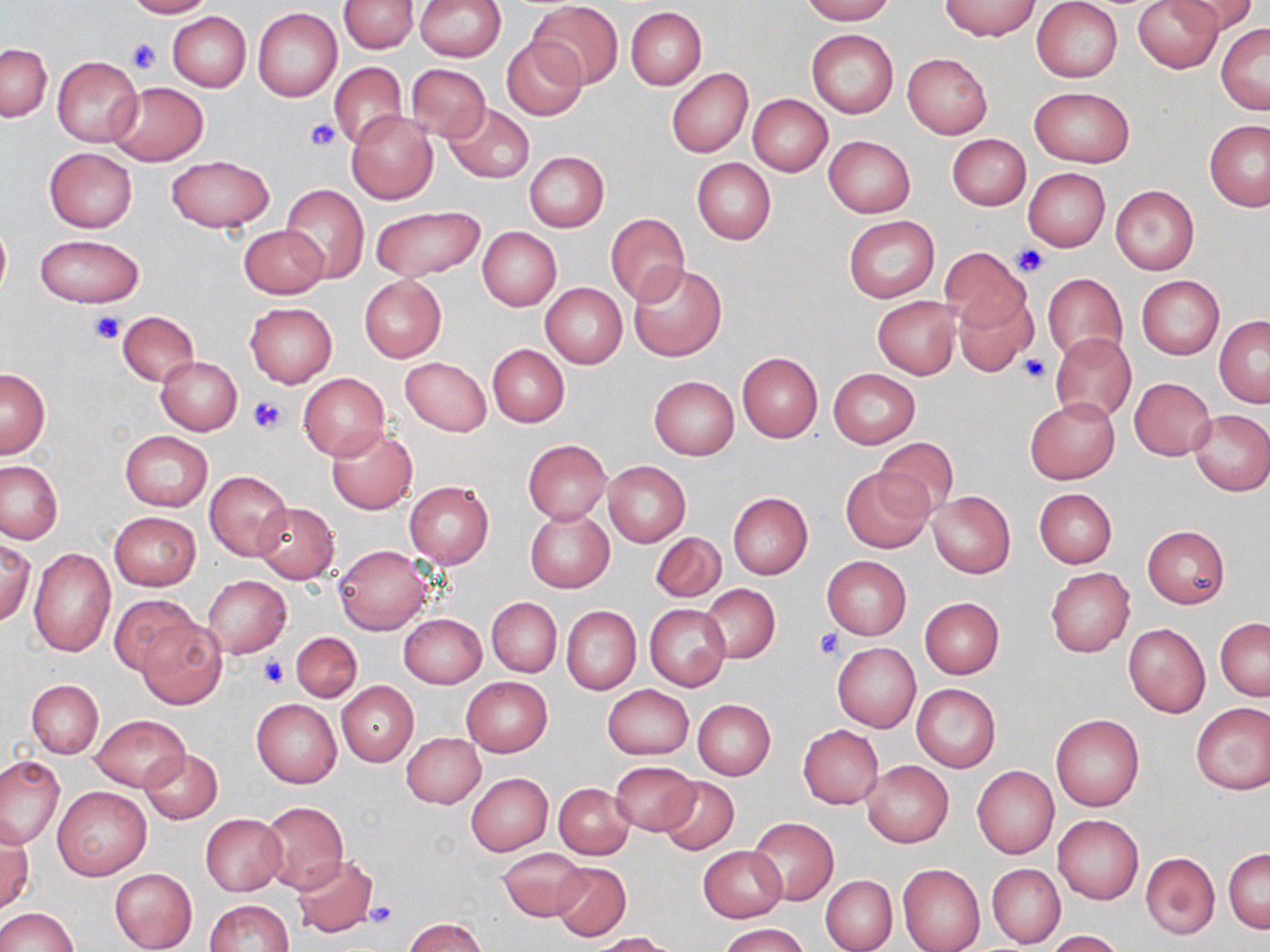
Summary:
  - Coordinate format: approximate bounding boxes as (x1,y1)-(x2,y2) corner pairs in pixels
  - Platelet locations: (124,37)-(163,75), (304,118)-(340,152), (1011,246)-(1048,277), (90,312)-(126,345), (1018,353)-(1051,383), (248,395)-(286,434), (815,629)-(843,659), (258,654)-(288,688), (363,900)-(398,929)
  - Uninfected red blood cell locations: (120,0)-(214,18), (339,0)-(417,54), (415,0)-(506,61), (799,0)-(896,23), (938,0)-(1041,40), (1032,0)-(1122,82), (1132,0)-(1222,73), (1170,0)-(1258,36), (529,1)-(623,88), (626,6)-(705,89), (253,7)-(342,101), (169,13)-(251,91), (1216,23)-(1270,113), (806,29)-(899,119), (501,37)-(587,120), (1,43)-(51,122), (902,52)-(993,139), (52,55)-(143,147), (328,62)-(407,149), (405,63)-(491,142), (666,68)-(753,158), (107,82)-(208,166), (1030,86)-(1134,167), (747,94)-(833,177), (444,102)-(534,185), (347,112)-(437,203), (1204,120)-(1270,210), (947,134)-(1031,211), (823,135)-(916,217), (45,147)-(138,233), (524,152)-(609,232), (165,155)-(275,232), (692,158)-(776,244), (1022,168)-(1110,252), (280,184)-(368,285), (1110,185)-(1199,275), (371,206)-(485,283), (606,213)-(690,306), (843,214)-(939,303), (0,218)-(10,301), (861,219)-(947,377), (239,224)-(329,298), (477,227)-(561,311), (36,234)-(144,308), (939,249)-(1029,329), (627,263)-(726,362), (1043,274)-(1127,361), (359,275)-(446,361), (1136,276)-(1223,358), (540,283)-(627,368), (953,293)-(1036,377), (873,296)-(958,379), (245,303)-(336,387), (115,310)-(199,386), (1214,315)-(1270,407), (1051,335)-(1136,422), (487,344)-(569,426), (737,352)-(822,443), (156,356)-(242,435), (401,356)-(491,437), (0,368)-(49,458), (828,369)-(920,448), (298,372)-(390,461), (649,376)-(740,459), (1130,377)-(1216,460), (1025,398)-(1120,484), (1188,408)-(1270,494), (327,427)-(418,515), (119,430)-(213,511), (874,437)-(960,518), (523,440)-(612,523), (0,460)-(64,544), (603,461)-(690,546), (841,467)-(934,553), (203,470)-(292,560), (403,481)-(493,570), (1034,488)-(1116,568), (928,492)-(1015,578), (728,493)-(812,579), (253,502)-(339,582), (526,508)-(613,593), (110,511)-(200,590), (1142,526)-(1229,608), (650,532)-(725,602), (0,538)-(34,624), (333,545)-(434,634), (28,549)-(115,658), (821,555)-(912,639), (1045,567)-(1135,657), (203,576)-(292,659), (701,584)-(780,663), (109,595)-(201,676), (919,597)-(1004,678), (486,598)-(561,676), (644,604)-(730,691), (561,606)-(641,695), (399,614)-(486,688), (1216,619)-(1270,700), (138,620)-(226,709), (1123,623)-(1210,717), (290,631)-(361,701), (832,642)-(920,732), (462,676)-(552,756), (27,679)-(104,758), (336,681)-(418,766), (912,683)-(1001,771), (602,685)-(694,760), (252,698)-(342,788), (692,699)-(775,780), (1191,703)-(1270,796), (89,714)-(189,792), (1051,714)-(1144,811), (798,724)-(883,808), (402,732)-(486,808), (140,748)-(223,824), (0,755)-(64,850), (609,760)-(699,835), (862,760)-(953,848), (972,766)-(1059,859), (466,773)-(552,855), (657,777)-(739,854), (553,783)-(634,859), (52,785)-(151,880), (260,801)-(348,893), (200,813)-(286,895), (1053,815)-(1143,904), (748,816)-(838,905), (0,822)-(32,917), (697,845)-(786,921), (498,848)-(587,921), (1224,848)-(1269,932), (1141,851)-(1220,939), (291,855)-(377,939), (552,861)-(631,941), (898,862)-(985,952), (987,864)-(1064,947), (109,868)-(197,951), (820,875)-(898,952), (203,900)-(294,952), (0,907)-(76,952), (404,917)-(485,952), (719,923)-(808,952), (1046,930)-(1124,952), (591,933)-(672,952)
  - Slide-level diagnosis: negative for blood parasites
  - Magnification: 1000x
  - Preparation: thin blood film
  - Field of view: one of a larger specimen
  - Stain: May-Grünwald-Giemsa
  - Modality: light microscopy
  - Image size: 1270×952 pixels